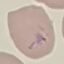

{
  "result": "malaria parasites detected",
  "preparation": "thin blood smear",
  "capture": "smartphone camera at the microscope eyepiece",
  "stain": "Giemsa",
  "image_type": "cell patch, automatically extracted from a larger field of view and resized to 64 × 64 pixels"
}